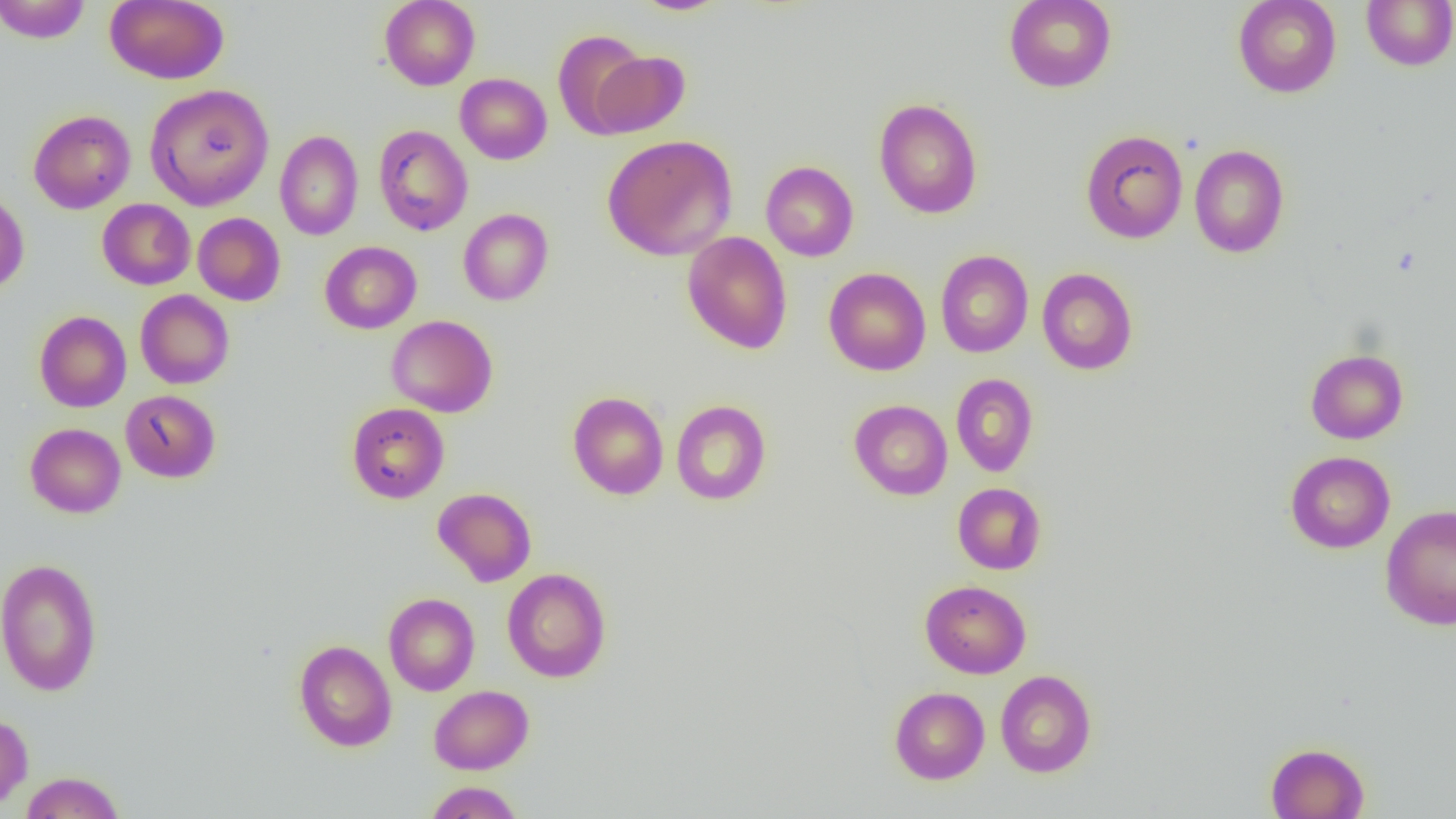
Summary:
  - Coordinate format: approximate bounding boxes as [x1, y1, x2, y2] in pixels
  - Uninfected red blood cell locations: [0, 0, 91, 43], [104, 0, 228, 84], [379, 0, 480, 90], [630, 0, 732, 16], [1004, 0, 1116, 92], [1232, 0, 1342, 98], [1361, 0, 1456, 71], [552, 30, 650, 137], [588, 51, 689, 137], [455, 73, 552, 164], [145, 84, 274, 211], [873, 98, 983, 218], [28, 109, 136, 214], [373, 124, 473, 236], [1080, 129, 1188, 244], [274, 130, 363, 240], [602, 135, 738, 261], [1189, 144, 1290, 258], [760, 161, 859, 261], [0, 191, 29, 295], [97, 198, 195, 290], [458, 208, 553, 306], [193, 213, 285, 306], [682, 231, 793, 354], [320, 241, 421, 334], [935, 250, 1033, 358], [823, 267, 931, 376], [1037, 268, 1138, 375], [135, 290, 234, 389], [34, 310, 131, 412], [386, 314, 498, 417], [1306, 349, 1408, 444], [950, 373, 1038, 476], [120, 390, 220, 483], [567, 392, 669, 499], [670, 399, 771, 505], [849, 399, 953, 500], [346, 402, 450, 503], [25, 423, 126, 518], [1285, 451, 1395, 553], [952, 482, 1046, 574], [433, 487, 536, 587], [1381, 505, 1456, 631], [0, 557, 103, 697], [502, 567, 611, 682], [920, 580, 1031, 678], [384, 593, 480, 696], [294, 639, 397, 752], [995, 670, 1097, 777], [429, 685, 533, 774], [889, 686, 990, 784], [0, 713, 33, 810], [1265, 742, 1369, 819], [20, 771, 125, 818], [424, 781, 524, 819]
  - Slide-level diagnosis: no evidence of blood parasites
  - Magnification: 1000x
  - Modality: optical microscopy
  - Image size: 1456×819 pixels
  - Preparation: thin blood smear
  - Field of view: single